Report the malaria status of this cell.
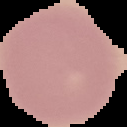
Uninfected.

image type = segmented cell region with the area outside set to black
preparation = thin blood film
image size = 127×127 pixels